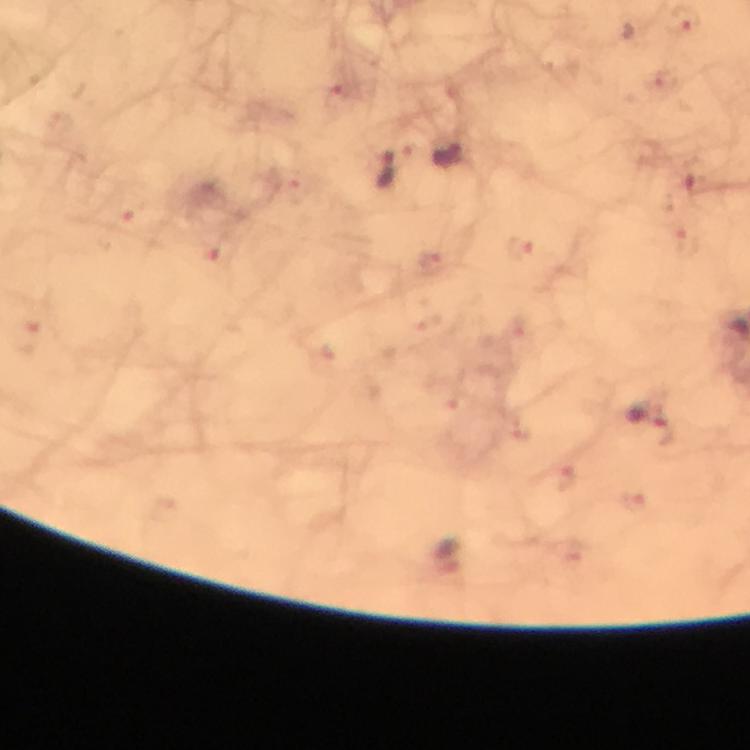

Approximate object centers, in pixels from the top-left corner. Malaria parasite locations: (x=687, y=20), (x=663, y=81), (x=335, y=95), (x=450, y=156), (x=385, y=169), (x=691, y=181), (x=125, y=206), (x=522, y=249), (x=217, y=256), (x=434, y=261), (x=28, y=336), (x=650, y=418), (x=554, y=482). 100x magnification. From a malaria diagnostic workup. Giemsa-stained preparation. Immersion oil applied. Image is 750×750 pixels. Cropped region of a single field of view. Thick smear. Photographed with a smartphone mounted on the microscope.